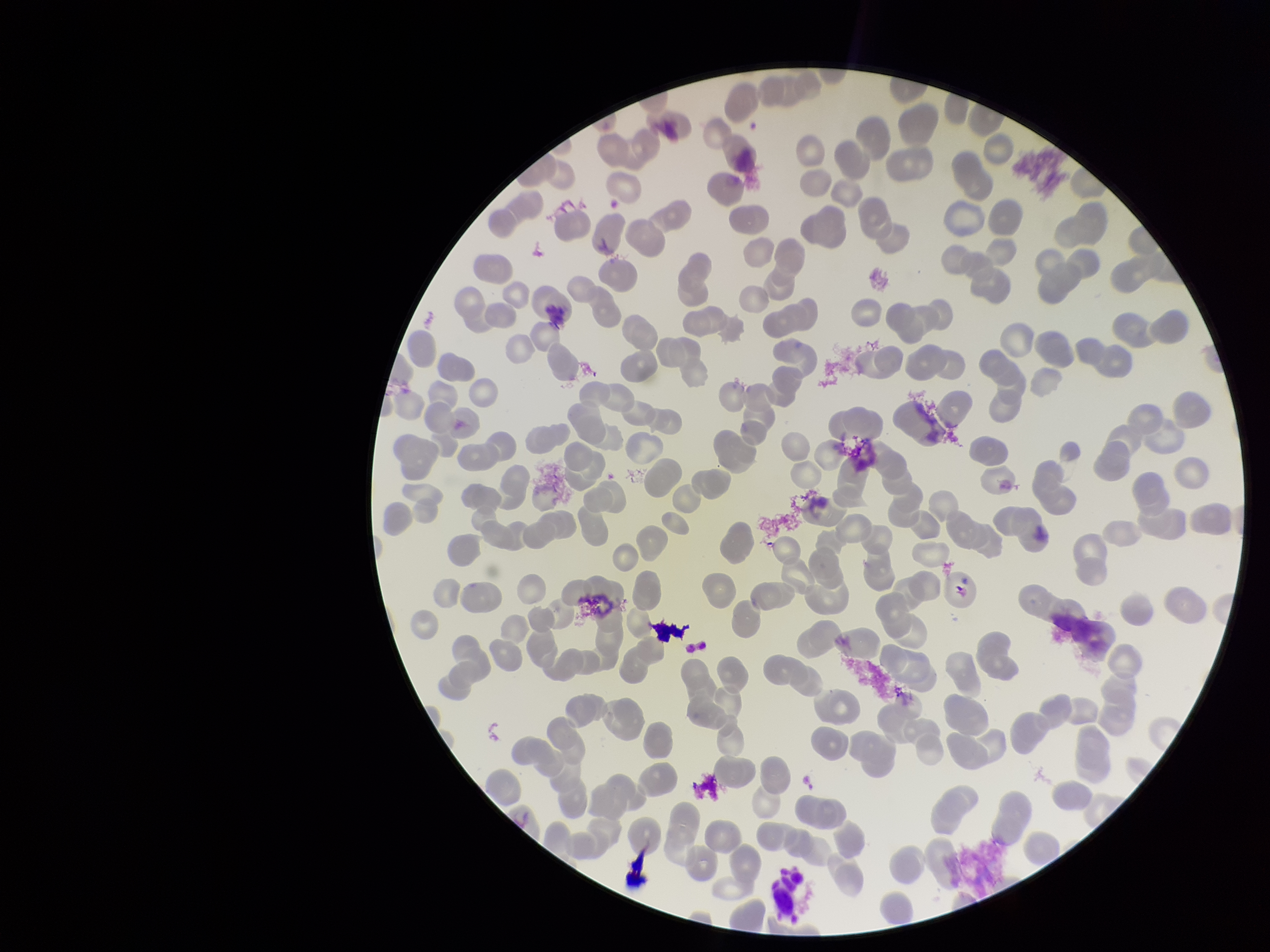
Patient malaria status: negative. Smartphone photograph taken through the eyepiece of a microscope. Single field of view. Parasitized red blood cell count: 0. Red blood cell count: 269. Giemsa stain. Parasitized red blood cells: none detected. Preparation: thin. Image is 1270×952 pixels.